Assess this cell for malaria.
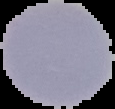
It is uninfected.

Cell region segmented out of the field of view; the surrounding area is masked to black. Image is 115×109 pixels. From a thin blood smear.